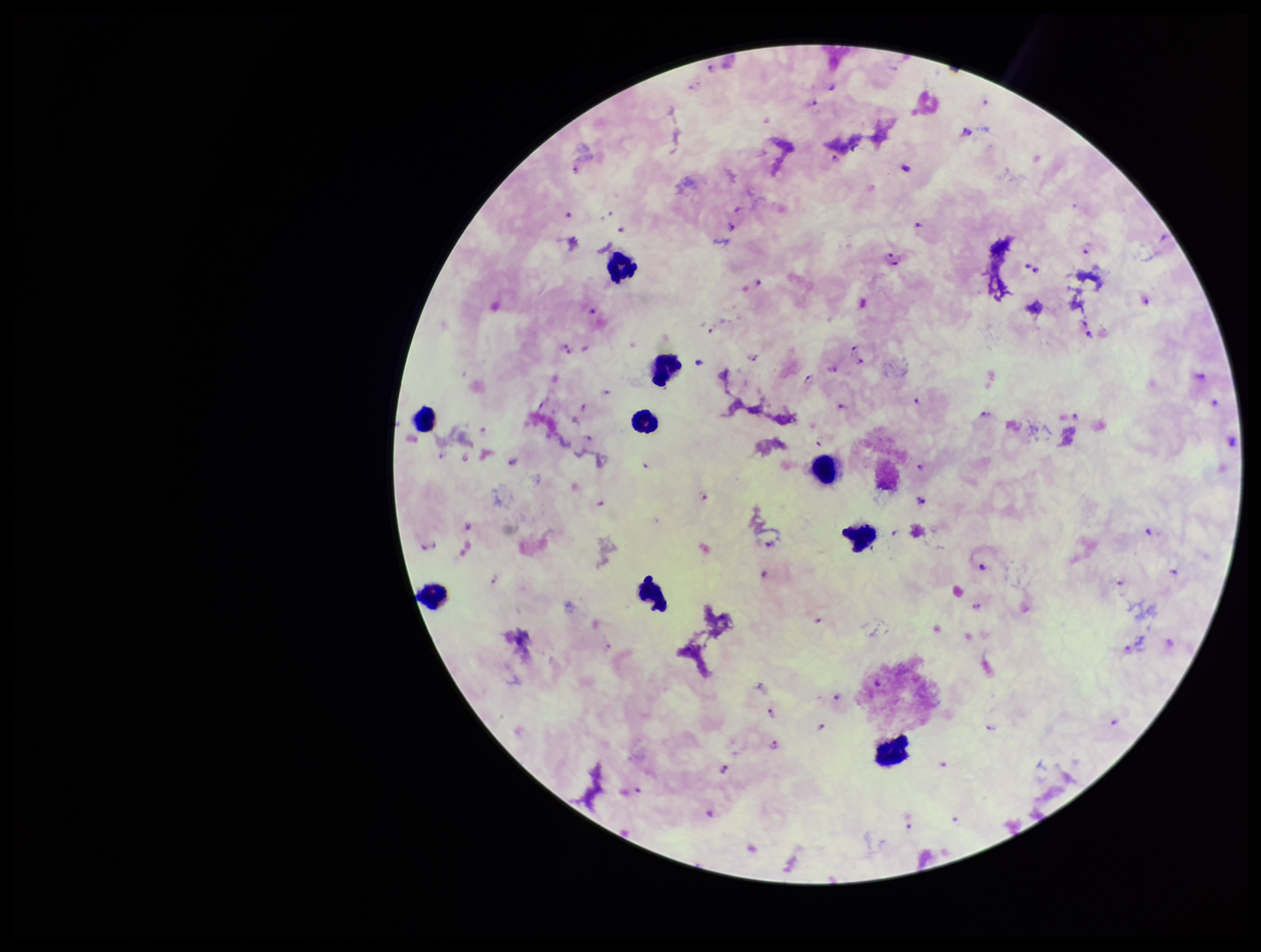
Summary:
  - Stain: Giemsa
  - Patient malaria status: positive
  - Plasmodium parasites: detected
  - Capture: smartphone photograph through the microscope eyepiece
  - Leukocyte count: 9
  - Preparation: thick
  - Image size: 1261×952 pixels
  - Field of view: one from this slide
  - Parasite count: 78
  - Species reported for this patient: Plasmodium falciparum